Give the extent of all Plasmodium falciparum-infected red blood cells.
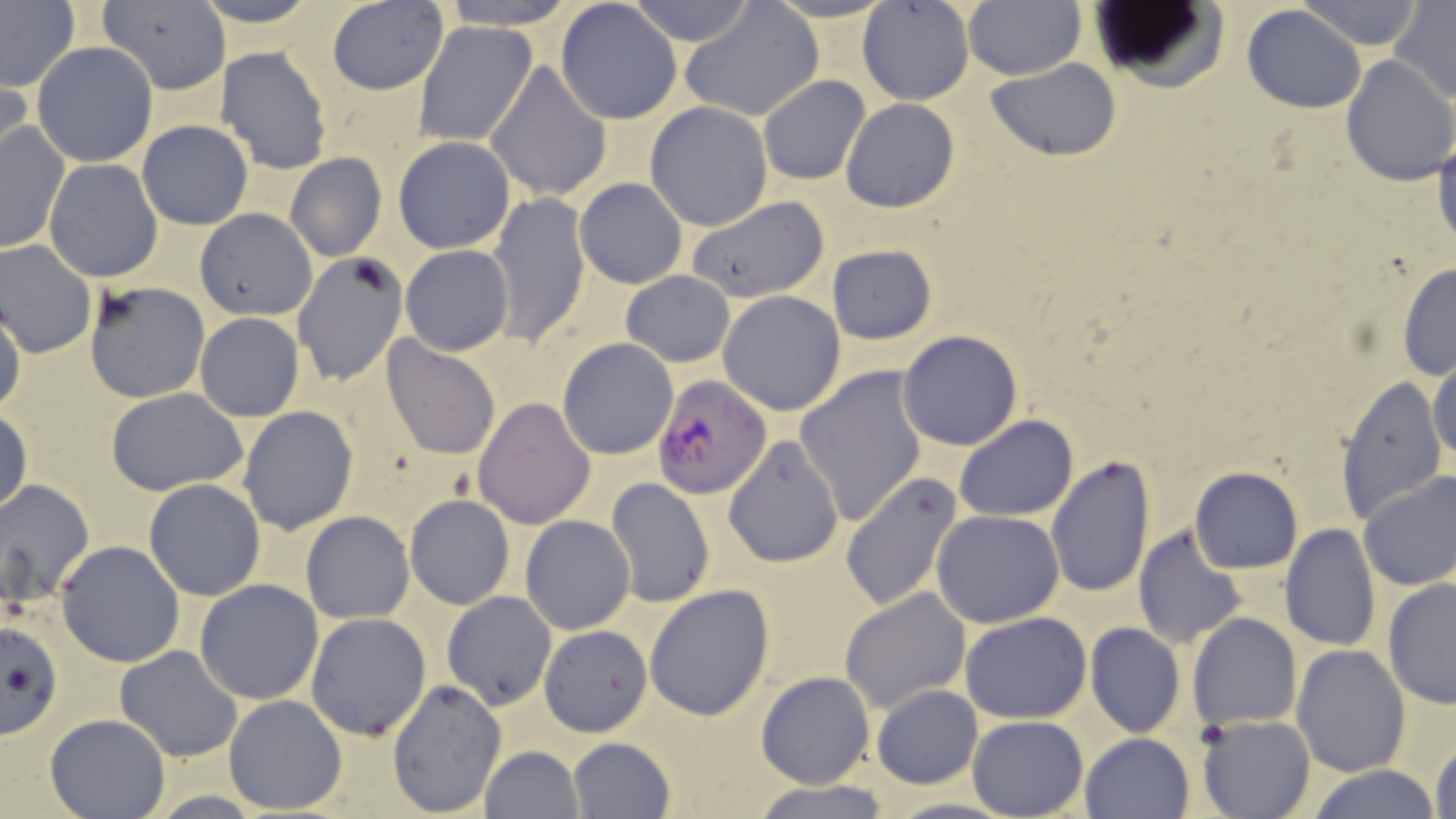

Approximate bounding boxes as [x1, y1, x2, y2] in pixels.
Plasmodium falciparum-infected red blood cells: [651, 375, 774, 498].

Uninfected red blood cell locations: [190, 0, 323, 27], [435, 0, 578, 29], [626, 0, 756, 47], [858, 0, 975, 106], [962, 0, 1087, 80], [1298, 0, 1424, 50], [0, 1, 80, 94], [97, 1, 232, 95], [326, 1, 450, 95], [554, 1, 683, 126], [681, 1, 823, 124], [1391, 1, 1456, 103], [1085, 4, 1226, 92], [1242, 5, 1367, 112], [413, 21, 537, 147], [31, 41, 160, 168], [215, 46, 335, 175], [1339, 54, 1455, 187], [986, 59, 1122, 161], [484, 60, 612, 203], [0, 63, 32, 172], [757, 74, 870, 186], [841, 98, 960, 213], [645, 101, 774, 231], [1, 120, 71, 256], [136, 120, 253, 230], [1431, 121, 1456, 256], [394, 136, 516, 253], [284, 152, 387, 262], [42, 159, 164, 282], [574, 176, 688, 288], [486, 192, 592, 347], [684, 195, 830, 303], [194, 207, 319, 321], [0, 240, 98, 359], [827, 244, 938, 345], [400, 245, 514, 355], [294, 255, 406, 388], [1396, 262, 1456, 380], [621, 271, 734, 368], [82, 281, 211, 403], [719, 291, 846, 416], [1, 303, 25, 418], [194, 313, 304, 422], [897, 330, 1023, 450], [381, 336, 502, 460], [556, 337, 679, 460], [1429, 353, 1455, 470], [795, 365, 928, 526], [1336, 373, 1447, 522], [105, 387, 250, 496], [473, 397, 596, 528], [238, 406, 358, 535], [0, 407, 32, 518], [954, 414, 1078, 521], [723, 436, 845, 569], [1045, 456, 1155, 599], [1189, 466, 1304, 574], [1356, 469, 1456, 591], [840, 471, 965, 611], [606, 477, 716, 607], [0, 478, 95, 615], [142, 479, 266, 601], [405, 495, 515, 610], [932, 509, 1065, 627], [301, 511, 414, 623], [519, 515, 635, 635], [1280, 524, 1381, 651], [1133, 525, 1246, 650], [56, 542, 185, 666], [1382, 577, 1456, 708], [194, 579, 324, 705], [645, 584, 775, 722], [840, 587, 970, 714], [441, 591, 557, 709], [305, 612, 432, 740], [961, 612, 1092, 724], [1188, 613, 1302, 731], [2, 615, 64, 744], [1085, 622, 1185, 739], [540, 624, 652, 737], [1291, 643, 1410, 776], [114, 646, 243, 762], [62, 665, 233, 796], [757, 672, 873, 788], [386, 678, 507, 817], [871, 686, 983, 788], [223, 693, 349, 812], [44, 714, 170, 819], [967, 714, 1089, 818], [1196, 715, 1318, 819], [1080, 732, 1196, 819], [568, 737, 676, 819], [1431, 739, 1456, 819], [480, 744, 583, 819], [1304, 765, 1439, 819], [752, 780, 894, 819]. Slide-level diagnosis: Plasmodium falciparum. 1000x magnification. Image is 1456×819 pixels. May-Grünwald-Giemsa-stained preparation. Single field of view. Thin blood film. Optical microscopy.